Name the cell type shown.
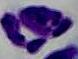
This is a leukocyte.

magnification: 1000x
modality: photomicrograph